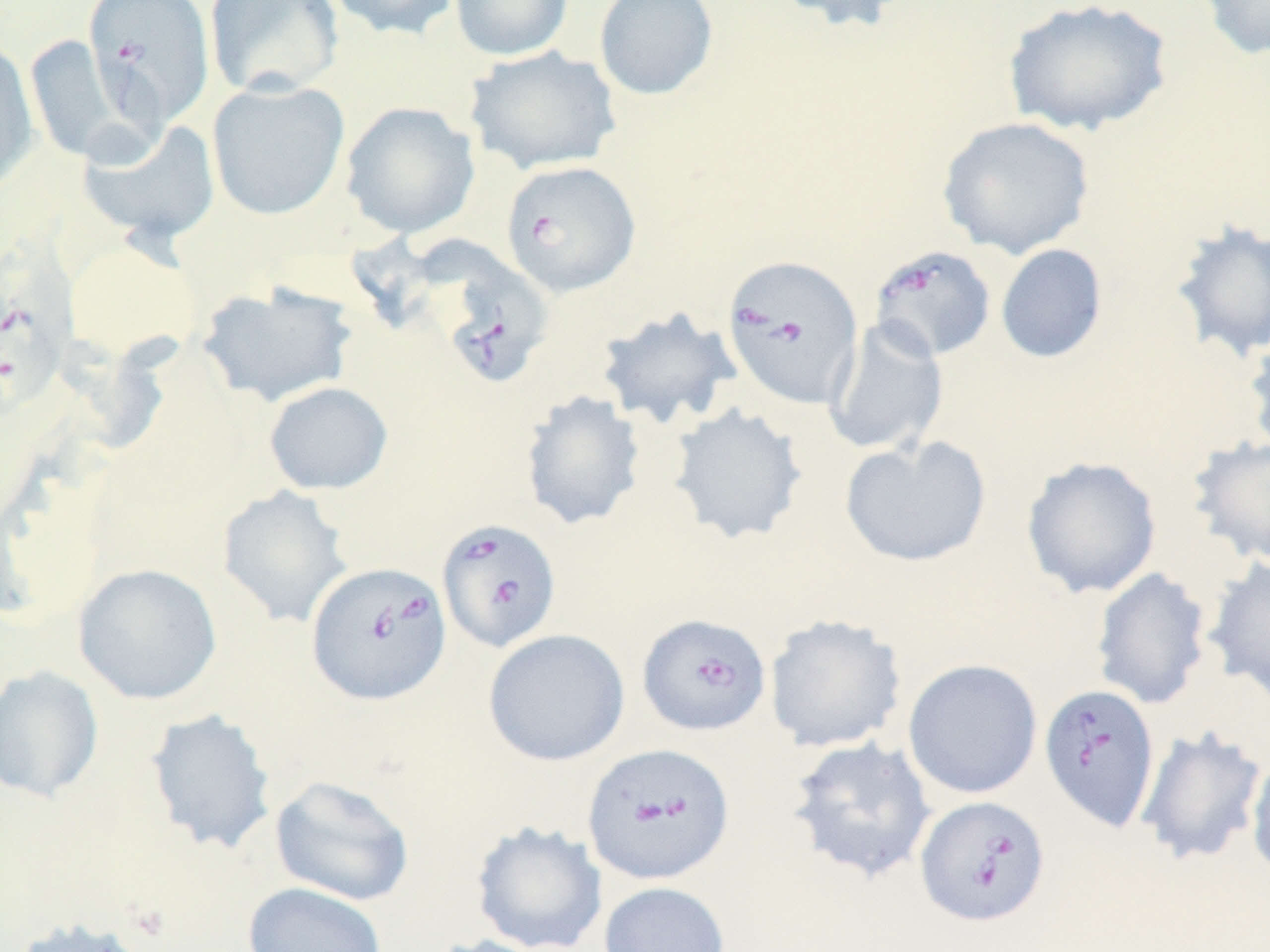

Summary:
  - Coordinate format: approximate bounding boxes as (x1,y1)-(x2,y2) corner pairs in pixels
  - Uninfected red blood cell locations: (204,0)-(344,99), (325,0)-(462,40), (450,0)-(573,61), (593,0)-(719,101), (773,0)-(917,34), (1002,0)-(1173,138), (1194,0)-(1270,61), (26,35)-(121,164), (0,40)-(39,194), (465,46)-(621,176), (207,79)-(350,220), (340,101)-(481,238), (936,115)-(1096,260), (78,118)-(221,245), (1169,219)-(1270,364), (64,240)-(198,362), (995,243)-(1107,364), (196,281)-(359,407), (595,306)-(742,430), (822,316)-(949,457), (1242,326)-(1270,460), (263,381)-(393,495), (519,390)-(646,531), (667,403)-(809,545), (839,434)-(992,568), (1186,434)-(1270,567), (1020,456)-(1162,599), (216,485)-(353,629), (1202,555)-(1270,704), (73,562)-(222,705), (1091,567)-(1213,711), (763,613)-(907,753), (482,629)-(630,767), (902,658)-(1043,800), (0,664)-(105,804), (144,708)-(278,855), (1134,725)-(1268,868), (785,736)-(938,885), (1245,753)-(1270,883), (270,775)-(415,907), (471,822)-(608,952), (597,881)-(731,952), (242,882)-(388,952), (8,917)-(156,952), (420,934)-(551,952)
  - Babesia divergens-infected red blood cell locations: (84,0)-(216,127), (500,160)-(641,297), (869,245)-(997,362), (0,246)-(76,423), (426,247)-(551,392), (720,254)-(864,409), (438,518)-(565,653), (308,559)-(454,705), (637,614)-(771,736), (1038,682)-(1161,831), (581,745)-(734,888), (915,795)-(1051,928)
  - Slide-level diagnosis: Babesia divergens
  - Field of view: single
  - Stain: May-Grünwald-Giemsa
  - Magnification: 1000x
  - Modality: optical microscopy
  - Image size: 1270×952 pixels
  - Preparation: thin blood film